Locate and identify every blood parasite.
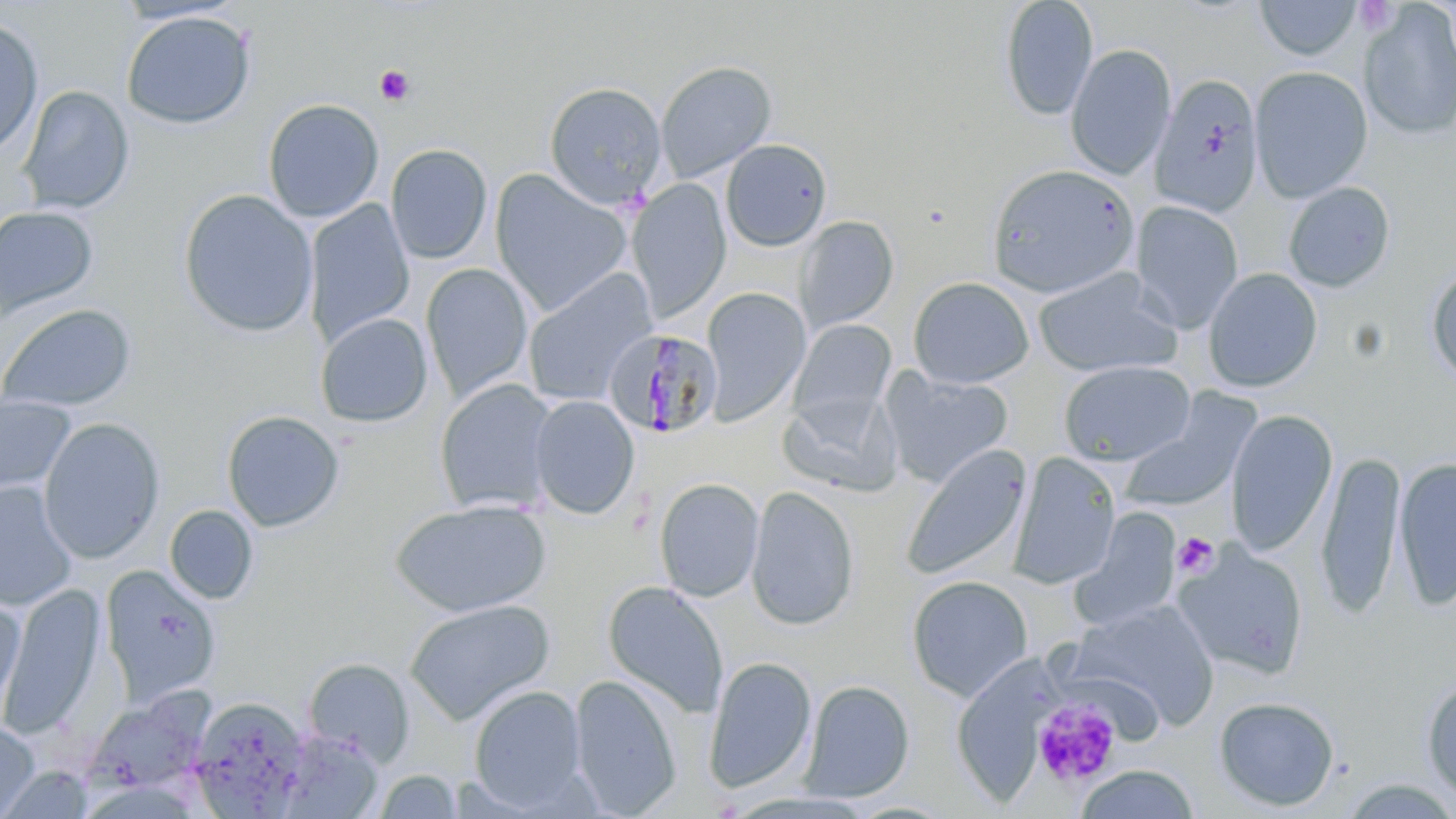

Approximate bounding boxes as [x1, y1, x2, y2] in pixels.
Plasmodium malariae-infected red blood cells: [603, 327, 724, 438].
No Plasmodium falciparum, Plasmodium ovale, Plasmodium vivax, Babesia divergens, or Trypanosoma brucei observed.

Uninfected red blood cell locations: [999, 0, 1099, 121], [1254, 0, 1363, 61], [1360, 3, 1456, 141], [121, 10, 256, 129], [0, 18, 43, 160], [1065, 43, 1176, 180], [655, 60, 777, 183], [1250, 66, 1373, 202], [1150, 73, 1264, 218], [544, 81, 667, 210], [18, 85, 134, 214], [263, 98, 384, 222], [720, 138, 832, 251], [385, 143, 493, 264], [985, 163, 1140, 299], [489, 169, 633, 317], [626, 178, 731, 322], [1283, 181, 1396, 292], [178, 189, 318, 337], [304, 199, 415, 347], [1129, 200, 1244, 334], [0, 206, 98, 321], [794, 215, 899, 334], [421, 263, 534, 403], [1426, 266, 1456, 387], [1033, 267, 1183, 378], [1202, 267, 1323, 393], [522, 269, 656, 406], [908, 276, 1034, 389], [700, 286, 812, 426], [0, 303, 137, 414], [316, 313, 433, 428], [789, 319, 897, 431], [1058, 360, 1196, 466], [880, 369, 1014, 488], [434, 378, 557, 515], [780, 391, 901, 497], [529, 394, 640, 519], [1117, 394, 1259, 515], [0, 396, 76, 495], [1225, 409, 1338, 557], [222, 410, 345, 532], [38, 418, 165, 563], [900, 444, 1031, 582], [1316, 448, 1407, 618], [1009, 451, 1122, 589], [1393, 456, 1455, 609], [653, 477, 764, 602], [0, 481, 78, 610], [746, 484, 860, 631], [390, 499, 551, 617], [165, 505, 259, 604], [1071, 506, 1183, 632], [1172, 542, 1309, 680], [101, 565, 220, 705], [906, 575, 1034, 702], [602, 580, 728, 719], [3, 584, 105, 738], [0, 595, 26, 725], [404, 598, 556, 725], [1068, 599, 1220, 730], [703, 655, 817, 795], [303, 658, 414, 765], [569, 674, 682, 817], [1421, 676, 1456, 804], [800, 679, 915, 801], [469, 685, 589, 811], [84, 691, 214, 800], [1213, 695, 1340, 812], [189, 696, 310, 815], [0, 721, 39, 819], [277, 728, 383, 818], [1074, 764, 1201, 819], [373, 769, 463, 818]. Platelet locations: [1354, 1, 1402, 37], [375, 65, 415, 107], [1173, 531, 1220, 579], [1032, 699, 1121, 788]. Slide-level diagnosis: Plasmodium malariae. Optical microscopy. May-Grünwald-Giemsa stain. One field of a larger specimen. Thin blood smear. 1000x magnification. Image is 1456×819 pixels.